Describe the morphology of the erythrocytes.
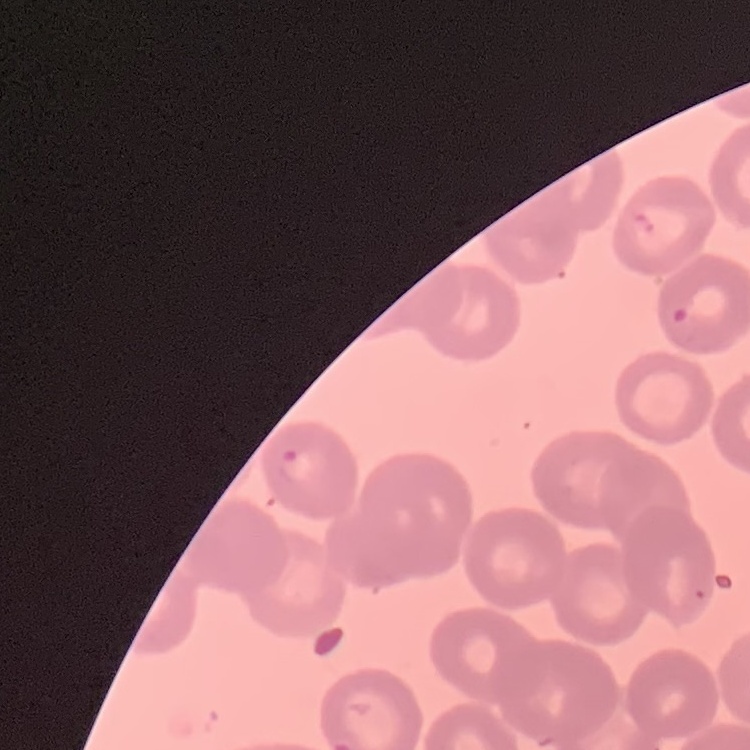
No rouleaux formation.

{
  "image_type": "one tile cut from a larger photomicrograph",
  "preparation": "thin peripheral smear",
  "stain": "Field's or Giemsa"
}